Assess this cell for malaria.
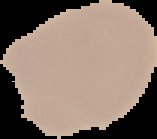
It is uninfected.

Summary:
  - Image type: segmented cell region on a black background
  - Preparation: thin blood smear
  - Image size: 157×139 pixels